Classify this cell by malaria status.
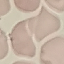

It is uninfected.

Summary:
  - Capture: smartphone through the microscope eyepiece
  - Stain: Giemsa
  - Image type: automatically extracted cell patch, resized to 64 × 64 pixels
  - Preparation: thin smear